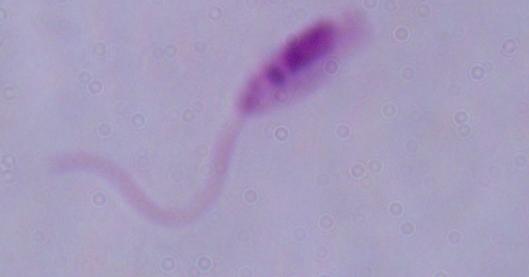
{
  "magnification": "1000x",
  "identification": "Leishmania",
  "modality": "micrograph"
}